Classify this cell by malaria status.
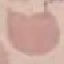
It is uninfected.

Summary:
  - Stain: Giemsa
  - Image type: cell patch, automatically extracted from a larger field of view and resized to 64 × 64 pixels
  - Preparation: thin blood smear
  - Capture: smartphone through the microscope eyepiece